Give the preparation type.
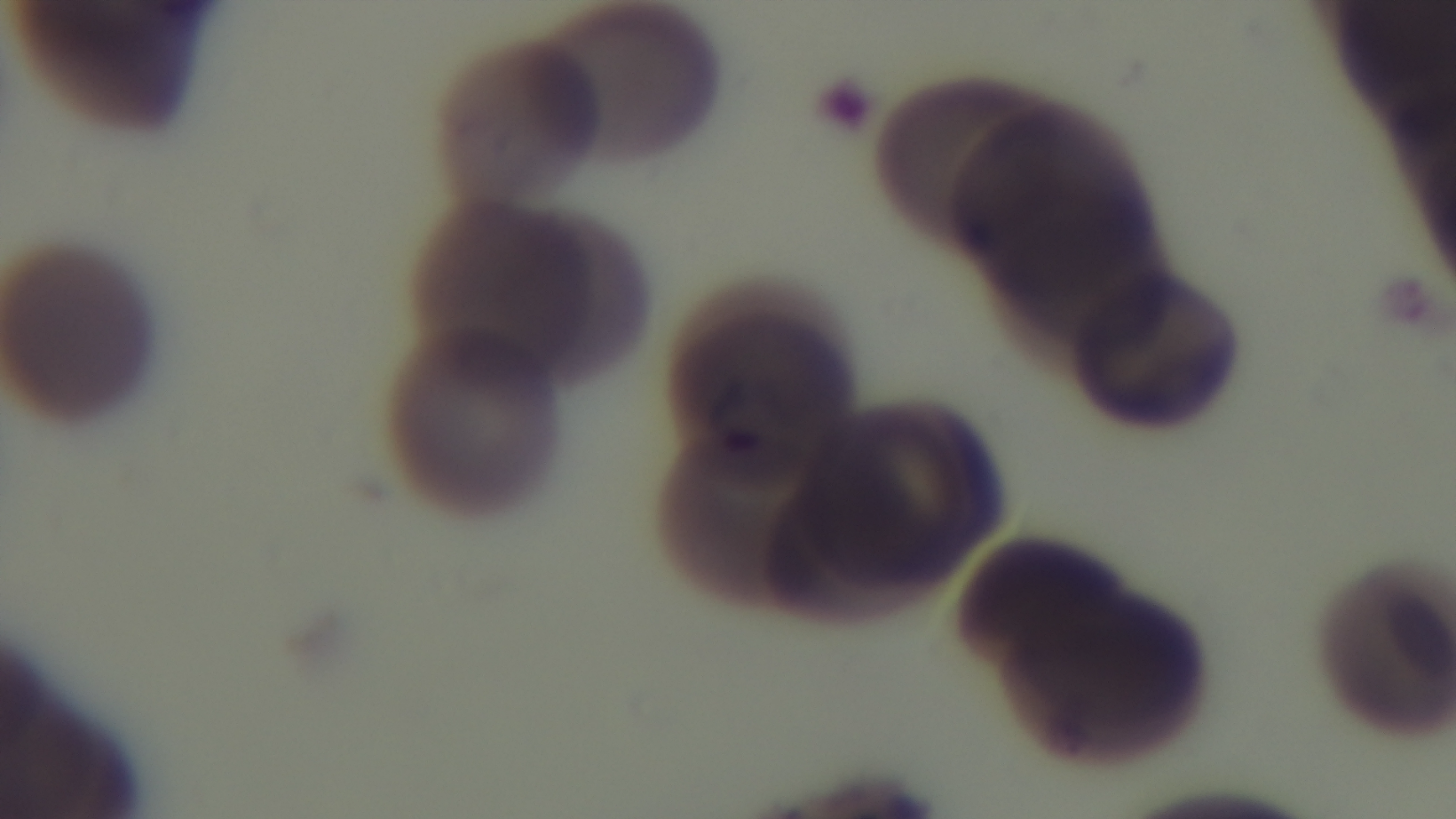
It is a thin blood film.

100x oil-immersion objective. Giemsa-stained. Photomicrograph. Captured with a mounted 4K digital camera. Malaria status: positive. One field from the slide.